Give the extent of all Plasmodium ovale-infected red blood cells.
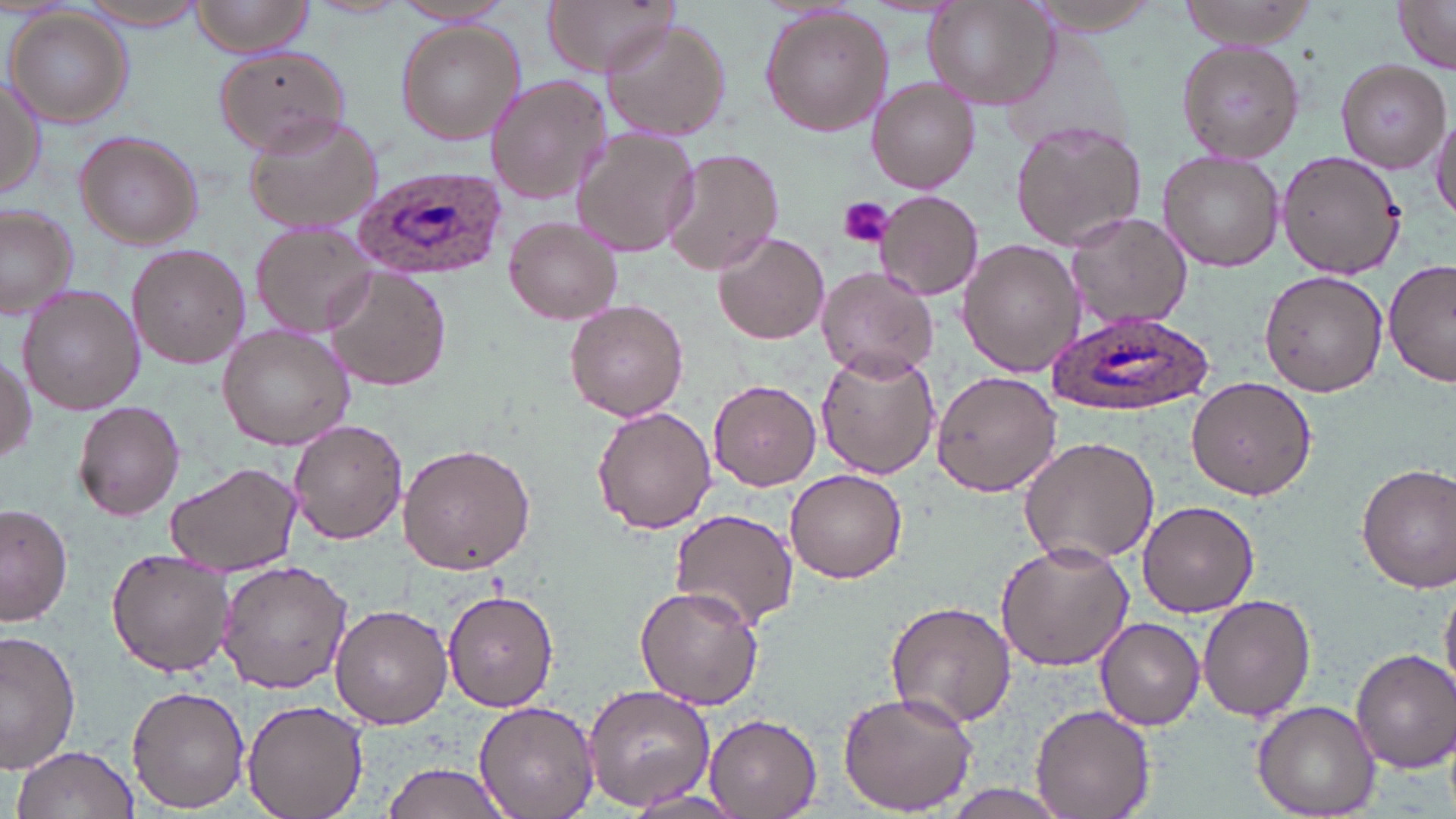
Approximate bounding boxes as (x1,y1)-(x2,y2) corner pairs in pixels.
Plasmodium ovale-infected red blood cells: (356,165)-(507,282), (1048,308)-(1213,417).

slide_level_diagnosis: Plasmodium ovale
platelet_locations: 'approximate bounding boxes as (x1,y1)-(x2,y2) corner pairs in pixels: (836,196)-(895,249)'
uninfected_red_blood_cell_locations: 'approximate bounding boxes as (x1,y1)-(x2,y2) corner pairs in pixels: (71,0)-(216,28), (187,0)-(320,57), (543,0)-(682,77), (923,0)-(1060,109), (1027,0)-(1174,36), (1177,0)-(1322,48), (1392,2)-(1456,74), (760,6)-(892,137), (5,8)-(134,129), (601,18)-(732,140), (396,21)-(524,143), (1176,39)-(1306,164), (213,46)-(351,156), (1337,58)-(1451,173), (485,73)-(613,207), (0,75)-(47,202), (867,76)-(981,193), (243,111)-(385,237), (1429,111)-(1456,223), (1009,120)-(1148,251), (571,128)-(699,258), (74,131)-(204,247), (660,148)-(783,276), (1157,149)-(1285,273), (1277,151)-(1405,280), (875,189)-(984,301), (0,202)-(78,319), (1063,213)-(1192,330), (504,216)-(624,326), (251,223)-(385,340), (713,232)-(830,346), (957,239)-(1083,378), (126,245)-(252,370), (1384,259)-(1456,391), (816,266)-(939,381), (1258,267)-(1388,396), (328,269)-(451,391), (20,285)-(144,413), (564,299)-(689,421), (217,324)-(353,450), (815,350)-(941,479), (0,353)-(35,470), (931,369)-(1061,499), (1186,376)-(1317,500), (708,378)-(821,492), (73,400)-(187,522), (590,406)-(717,535), (287,420)-(407,545), (1017,433)-(1161,569), (398,442)-(539,575), (167,462)-(300,577), (1356,464)-(1456,590), (785,468)-(909,583), (1138,500)-(1259,617), (2,502)-(74,627), (669,509)-(800,629), (996,540)-(1134,672), (106,549)-(232,677), (215,557)-(356,692), (1440,584)-(1456,696), (634,586)-(764,713), (443,590)-(559,712), (1199,596)-(1317,722), (884,601)-(1017,729), (330,604)-(452,728), (1097,616)-(1205,730), (0,629)-(78,775), (1352,648)-(1454,772), (582,681)-(717,811), (127,685)-(249,812), (838,688)-(978,815), (242,697)-(368,819), (472,701)-(601,819), (1251,701)-(1382,818), (1031,704)-(1154,819), (703,715)-(823,819), (11,744)-(139,819), (383,761)-(515,819), (934,784)-(1075,818), (626,791)-(748,817)'
field_of_view: one of a larger specimen
modality: light microscopy
preparation: thin blood film
image_size: 1456×819 pixels
stain: May-Grünwald-Giemsa
magnification: 1000x